Report the malaria status.
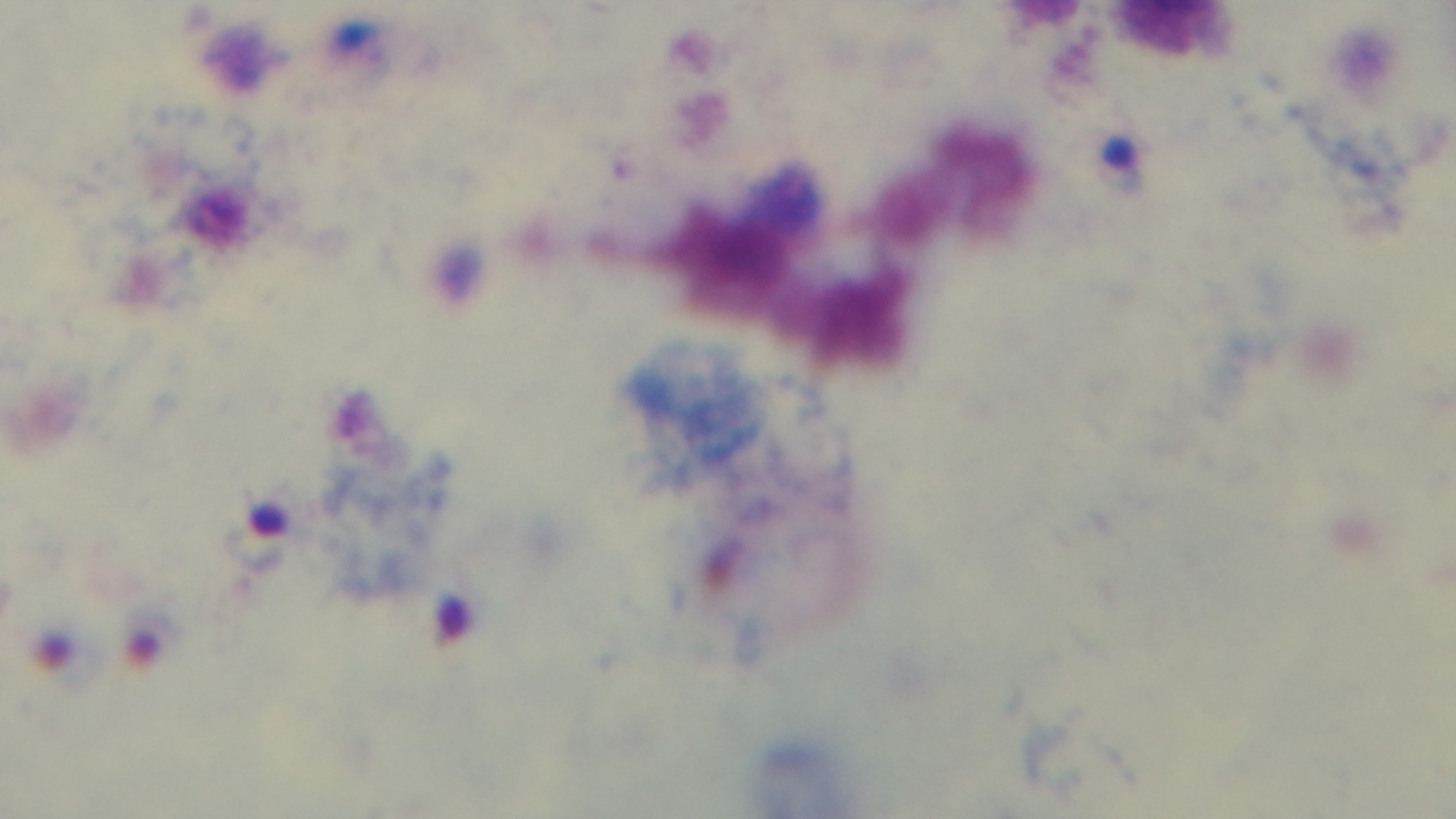

Infected.

field_of_view: one from the slide
stain: Giemsa
objective: 100x oil immersion
preparation: thick blood film
capture: mounted 4K digital camera
modality: light microscopy